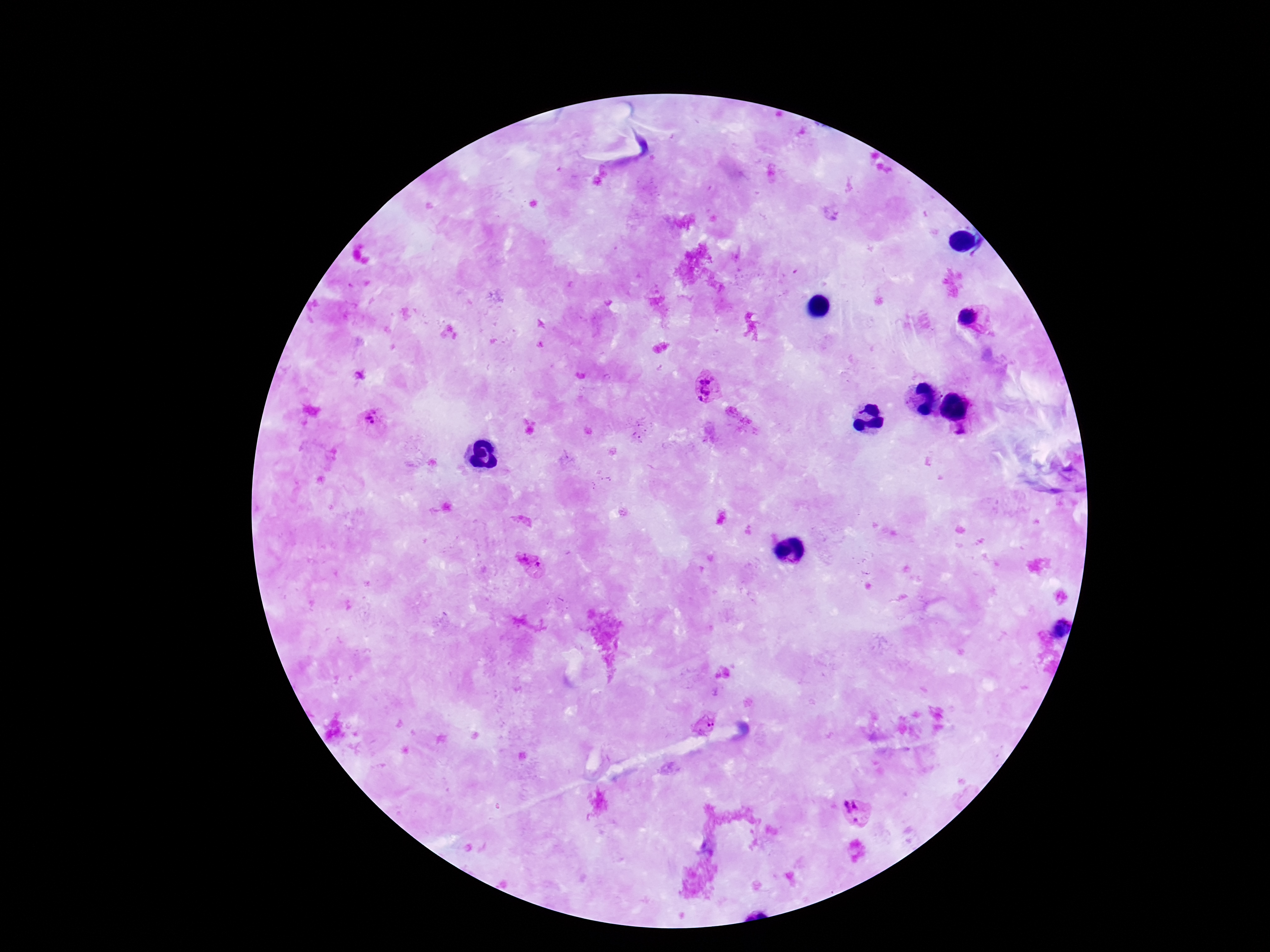 Approximate centers as [x, y] in pixels. Plasmodium parasite locations: [967, 315], [707, 388], [370, 418], [962, 433], [525, 557], [538, 564], [707, 725], [857, 812]. Patient malaria status: positive. Giemsa-stained preparation. Image is 1270×952 pixels. Thick blood film. One field from this slide. 100x magnification. Photographed through the microscope eyepiece with a smartphone camera.